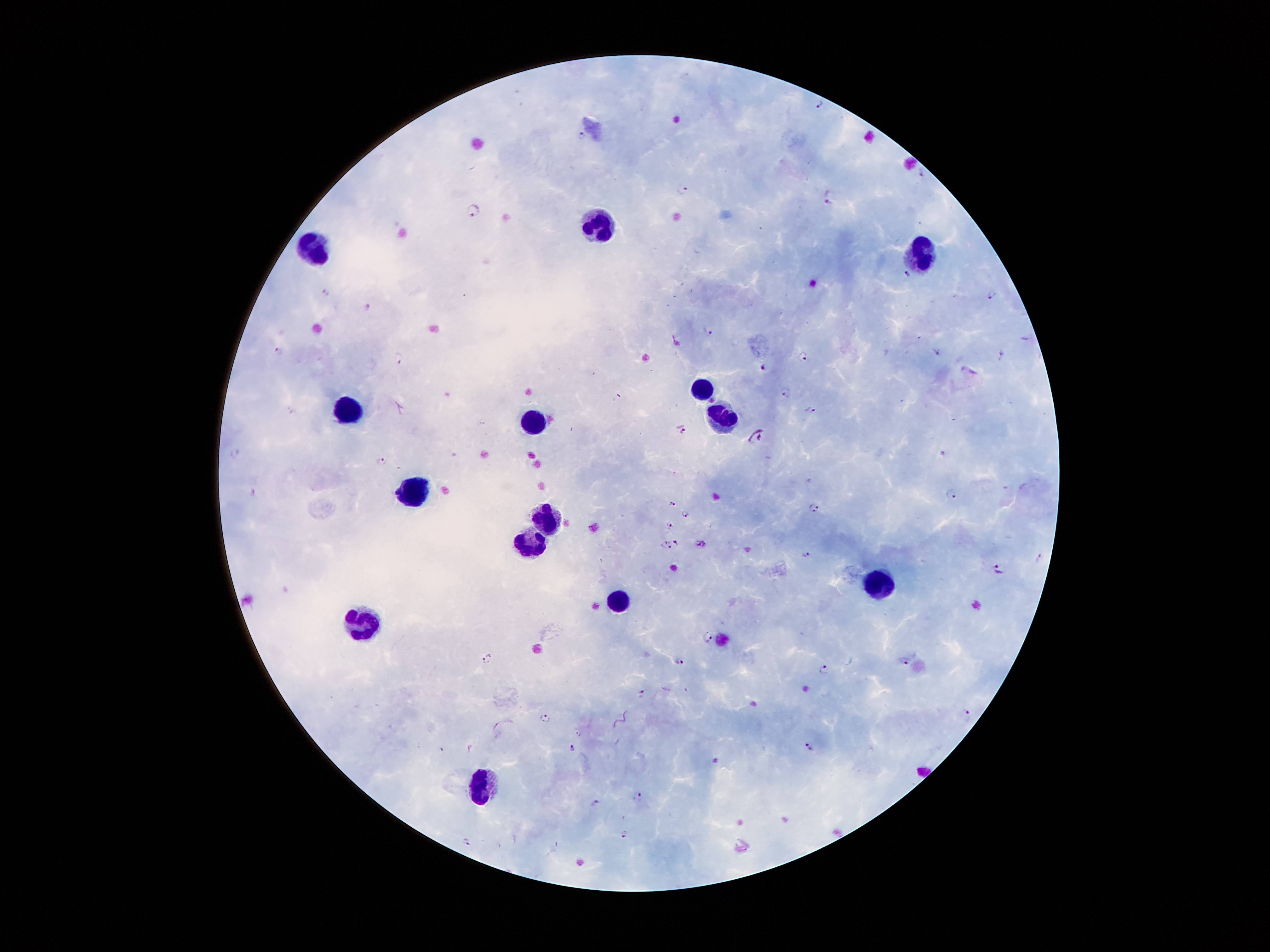

Approximate centers as [x, y] in pixels.
Summary:
  - Leukocyte locations: [598, 225], [311, 247], [926, 248], [704, 388], [343, 408], [726, 416], [536, 423], [418, 493], [547, 520], [531, 542], [879, 580], [620, 604], [363, 621], [479, 786]
  - Plasmodium parasite locations: [819, 102], [582, 134], [921, 173], [682, 189], [830, 196], [472, 210], [906, 273], [326, 292], [992, 296], [366, 308], [708, 332], [282, 351], [937, 352], [803, 356], [1003, 356], [400, 357], [764, 367], [787, 392], [810, 410], [682, 429], [755, 436], [235, 453], [382, 460], [254, 494], [952, 495], [672, 504], [813, 507], [687, 514], [668, 523], [676, 542], [667, 545], [701, 545], [808, 554], [1001, 569], [706, 636], [487, 660], [905, 660], [681, 661], [824, 669], [642, 693], [966, 715], [547, 718], [808, 746], [572, 749], [714, 760], [638, 797], [594, 801], [624, 833], [467, 841]
  - Field of view: one from this slide
  - Magnification: 100x
  - Capture: smartphone through the microscope eyepiece
  - Stain: Giemsa
  - Preparation: thick blood film
  - Patient malaria status: infected with Plasmodium falciparum
  - Image size: 1270×952 pixels